Name the blood parasite species.
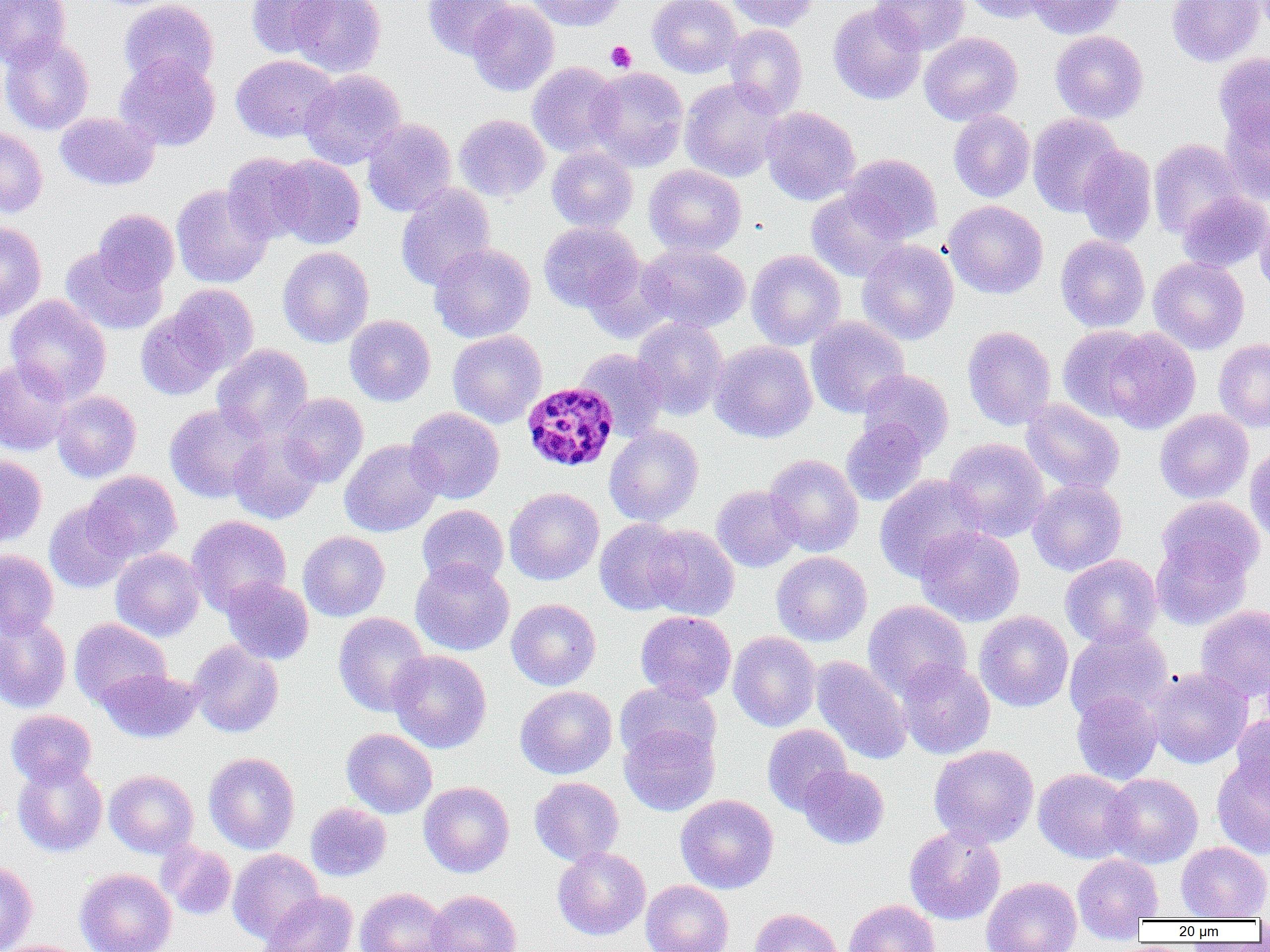

Plasmodium malariae.

Summary:
  - Coordinate format: approximate bounding boxes as [x1, y1, x2, y2] in pixels
  - Plasmodium malariae-infected red blood cell locations: [521, 382, 619, 472]
  - Platelet locations: [606, 41, 636, 72]
  - Uninfected red blood cell locations: [0, 0, 70, 69], [119, 0, 219, 88], [247, 0, 338, 58], [289, 0, 386, 77], [423, 0, 515, 59], [525, 0, 626, 31], [647, 0, 742, 78], [726, 0, 820, 32], [872, 0, 969, 55], [963, 0, 1055, 23], [1027, 0, 1124, 39], [1166, 0, 1265, 67], [467, 1, 559, 96], [828, 2, 926, 105], [724, 24, 808, 116], [1050, 30, 1148, 124], [919, 32, 1023, 125], [0, 35, 94, 135], [1213, 52, 1270, 146], [115, 54, 221, 151], [230, 54, 338, 143], [527, 62, 621, 157], [586, 67, 688, 171], [299, 69, 406, 169], [679, 78, 786, 182], [1220, 106, 1270, 202], [761, 107, 860, 205], [948, 109, 1035, 202], [55, 112, 159, 190], [1027, 113, 1124, 217], [454, 114, 550, 201], [362, 118, 457, 217], [0, 126, 47, 218], [1148, 138, 1246, 239], [547, 145, 638, 232], [1077, 145, 1157, 247], [222, 152, 314, 244], [842, 154, 942, 243], [271, 155, 366, 249], [644, 164, 746, 256], [171, 184, 273, 288], [395, 184, 496, 290], [806, 188, 909, 282], [1177, 192, 1269, 272], [943, 200, 1048, 299], [1255, 203, 1270, 302], [92, 209, 179, 293], [0, 221, 47, 321], [538, 221, 642, 312], [1055, 235, 1150, 332], [857, 239, 959, 345], [430, 243, 536, 343], [637, 243, 750, 333], [60, 244, 167, 335], [757, 245, 949, 346], [277, 246, 374, 347], [746, 249, 846, 350], [1148, 257, 1249, 354], [581, 258, 676, 344], [169, 283, 259, 373], [5, 295, 112, 403], [136, 307, 227, 401], [344, 315, 436, 406], [805, 316, 909, 418], [632, 317, 729, 420], [962, 325, 1057, 431], [1057, 325, 1154, 422], [1101, 328, 1201, 433], [447, 330, 546, 428], [1214, 338, 1270, 432], [709, 341, 817, 442], [212, 343, 313, 438], [574, 347, 668, 441], [0, 359, 72, 455], [857, 368, 954, 459], [52, 390, 141, 483], [277, 393, 368, 487], [1020, 399, 1125, 494], [164, 403, 270, 502], [406, 407, 504, 504], [1155, 409, 1254, 503], [841, 419, 929, 506], [604, 425, 704, 527], [229, 430, 323, 524], [944, 437, 1050, 541], [339, 439, 444, 537], [1244, 445, 1270, 545], [0, 453, 47, 547], [764, 454, 863, 557], [83, 471, 181, 562], [874, 474, 986, 581], [1027, 479, 1127, 576], [711, 485, 804, 572], [504, 487, 604, 585], [1157, 496, 1264, 582], [44, 500, 136, 593], [417, 504, 509, 589], [187, 515, 291, 616], [594, 518, 688, 615], [644, 524, 740, 621], [914, 526, 1025, 626], [298, 531, 390, 621], [1151, 536, 1253, 630], [110, 548, 205, 641], [0, 549, 59, 639], [772, 551, 872, 646], [1060, 554, 1162, 648], [410, 558, 515, 656], [221, 578, 314, 664], [506, 598, 601, 690], [863, 600, 972, 700], [1195, 605, 1270, 703], [635, 611, 736, 703], [974, 611, 1073, 712], [333, 612, 431, 716], [0, 615, 71, 713], [69, 618, 171, 709], [1064, 625, 1172, 724], [728, 632, 821, 731], [188, 640, 284, 738], [388, 650, 491, 753], [811, 656, 912, 765], [896, 658, 995, 759], [1148, 667, 1252, 769], [98, 669, 203, 743], [615, 681, 721, 767], [515, 685, 617, 779], [1071, 690, 1162, 785], [6, 710, 96, 787], [1232, 714, 1270, 807], [619, 723, 719, 816], [762, 724, 852, 815], [341, 728, 437, 818], [929, 744, 1039, 847], [204, 752, 300, 853], [1211, 755, 1270, 859], [12, 759, 107, 857], [798, 765, 889, 849], [1033, 769, 1135, 863], [104, 770, 199, 858], [1102, 773, 1203, 868], [529, 776, 624, 866], [418, 781, 515, 877], [675, 794, 778, 893], [305, 802, 391, 881], [904, 826, 1006, 925], [157, 842, 237, 920], [1176, 842, 1270, 920], [552, 847, 650, 940], [228, 849, 324, 945], [1072, 852, 1164, 936], [0, 860, 38, 952], [75, 868, 176, 952], [981, 876, 1081, 952], [641, 880, 733, 952], [355, 887, 451, 952], [426, 890, 521, 952], [260, 891, 358, 952], [844, 899, 941, 952], [750, 907, 844, 952]
  - Image size: 1270×952 pixels
  - Field of view: single
  - Modality: light microscopy
  - Magnification: 1000x
  - Preparation: thin blood film